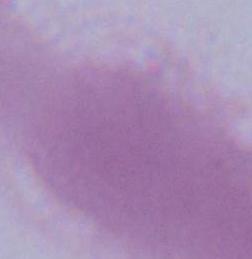

Captured at 1000x magnification. Micrograph. An erythrocyte is seen.